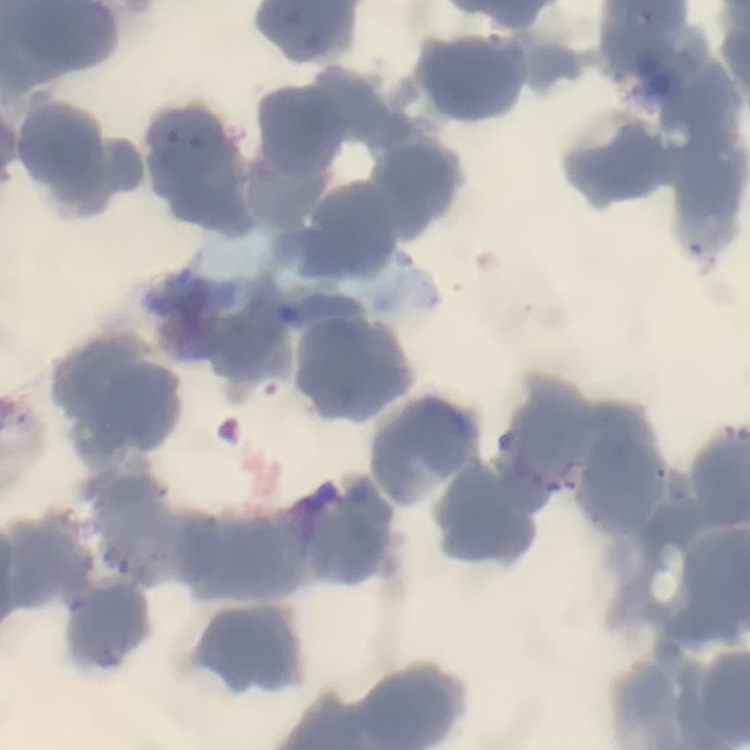

Summary:
  - Red blood cell morphology: rouleaux formation
  - Image type: square crop of a larger photomicrograph
  - Stain: Field's or Giemsa
  - Preparation: thin blood film